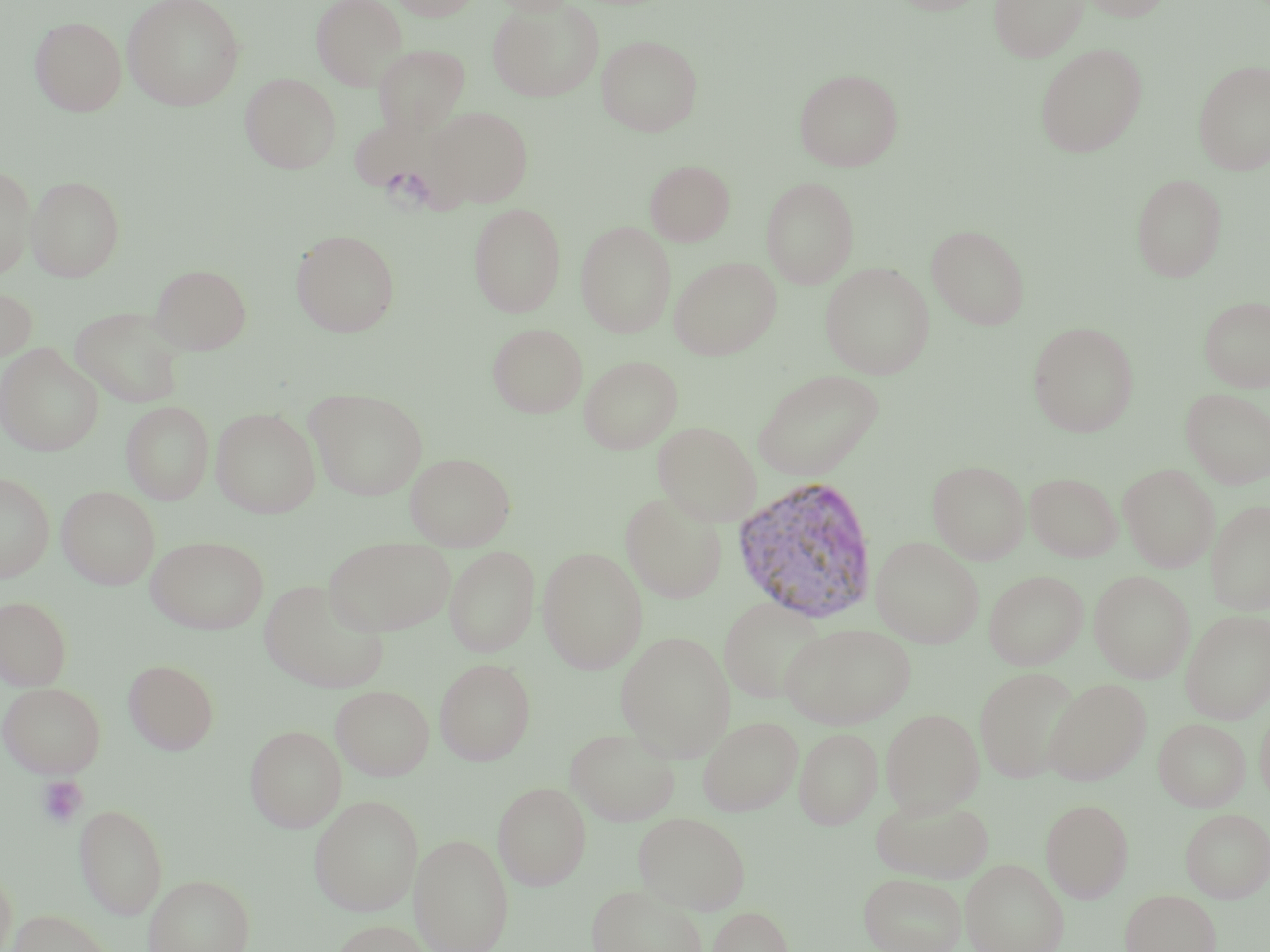

slide-level diagnosis = Plasmodium vivax
magnification = 1000x
uninfected red blood cell locations = approximate bounding boxes as (x1,y1)-(x2,y2) corner pairs in pixels: (122,0)-(245,110), (311,0)-(407,90), (391,0)-(483,20), (490,0)-(578,15), (889,0)-(991,15), (989,0)-(1088,62), (1077,0)-(1173,21), (488,2)-(605,101), (30,16)-(127,116), (596,34)-(703,137), (1035,43)-(1148,157), (373,44)-(470,136), (1193,59)-(1270,175), (794,69)-(904,172), (240,73)-(341,174), (425,106)-(533,208), (645,160)-(734,247), (0,165)-(37,279), (1131,173)-(1228,282), (26,175)-(125,282), (761,176)-(859,289), (469,203)-(565,317), (576,221)-(676,338), (926,224)-(1031,330), (291,229)-(400,337), (669,256)-(781,360), (819,262)-(935,379), (151,263)-(251,354), (0,286)-(37,362), (1199,296)-(1270,392), (70,307)-(187,408), (1027,321)-(1139,437), (488,323)-(587,418), (0,344)-(103,456), (579,355)-(682,454), (753,369)-(884,481), (305,388)-(428,500), (1182,388)-(1270,489), (121,401)-(213,505), (211,407)-(320,518), (653,420)-(761,525), (405,452)-(515,550), (927,460)-(1030,564), (1119,464)-(1219,572), (0,472)-(54,582), (1025,472)-(1122,562), (57,485)-(160,589), (620,492)-(727,604), (1206,500)-(1270,615), (146,536)-(268,634), (870,536)-(984,647), (323,537)-(456,636), (445,546)-(540,657), (538,548)-(648,673), (984,570)-(1088,670), (1088,570)-(1195,683), (259,580)-(389,692), (0,595)-(72,690), (719,596)-(829,704), (1181,609)-(1269,723), (780,622)-(916,729), (789,623)-(895,831), (616,631)-(736,761), (435,658)-(536,765), (123,659)-(218,755), (974,667)-(1081,783), (1044,678)-(1150,785), (0,682)-(105,777), (331,685)-(434,781), (1256,703)-(1270,810), (880,708)-(984,816), (698,715)-(803,816), (1154,718)-(1250,811), (245,725)-(346,832), (794,726)-(882,830), (565,727)-(680,825), (493,782)-(592,890), (309,795)-(423,915), (870,795)-(994,883), (1041,798)-(1133,902), (74,802)-(168,919), (1180,808)-(1270,902), (633,811)-(751,915), (410,833)-(513,952), (961,858)-(1068,952), (0,866)-(17,952), (858,871)-(967,952), (144,873)-(255,952), (586,884)-(710,952), (1121,889)-(1221,952), (707,905)-(794,952), (6,908)-(114,952), (330,919)-(433,952)
modality = light microscopy
field of view = single
image size = 1270×952 pixels
platelet locations = approximate bounding boxes as (x1,y1)-(x2,y2) corner pairs in pixels: (37,776)-(89,828)
Plasmodium vivax-infected red blood cell locations = approximate bounding boxes as (x1,y1)-(x2,y2) corner pairs in pixels: (731,475)-(880,625)
preparation = thin blood film
stain = May-Grünwald-Giemsa